Classify this cell by malaria status.
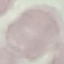
It is uninfected.

Thin blood smear. Cell patch, automatically extracted from a larger field of view and resized to 64 × 64 pixels. Acquired by smartphone through the microscope eyepiece. Giemsa-stained preparation.